Assess the morphology of the erythrocytes.
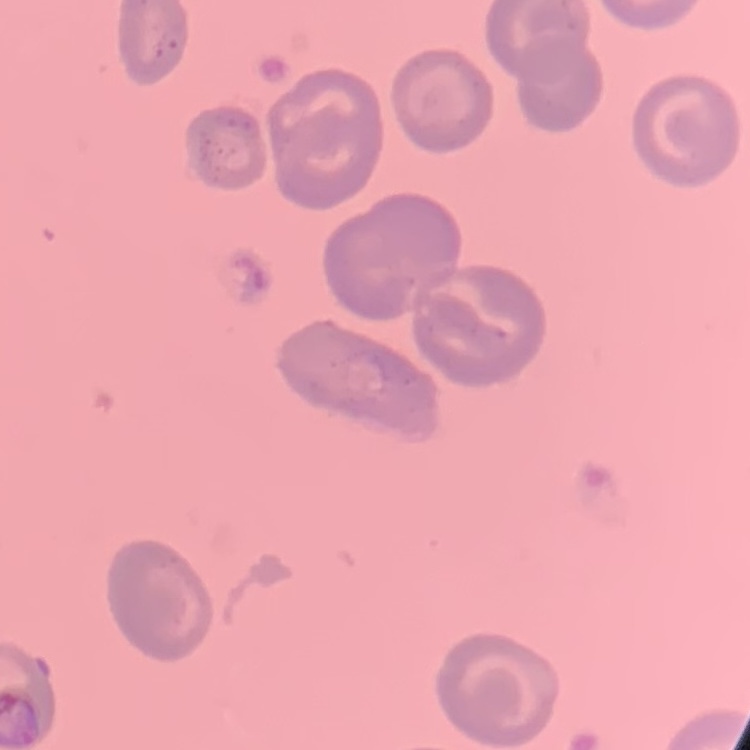

No rouleaux formation.

Thin peripheral smear. Field's or Giemsa stain. One tile cut from a larger photomicrograph.